Locate every leukocyte (white blood cell).
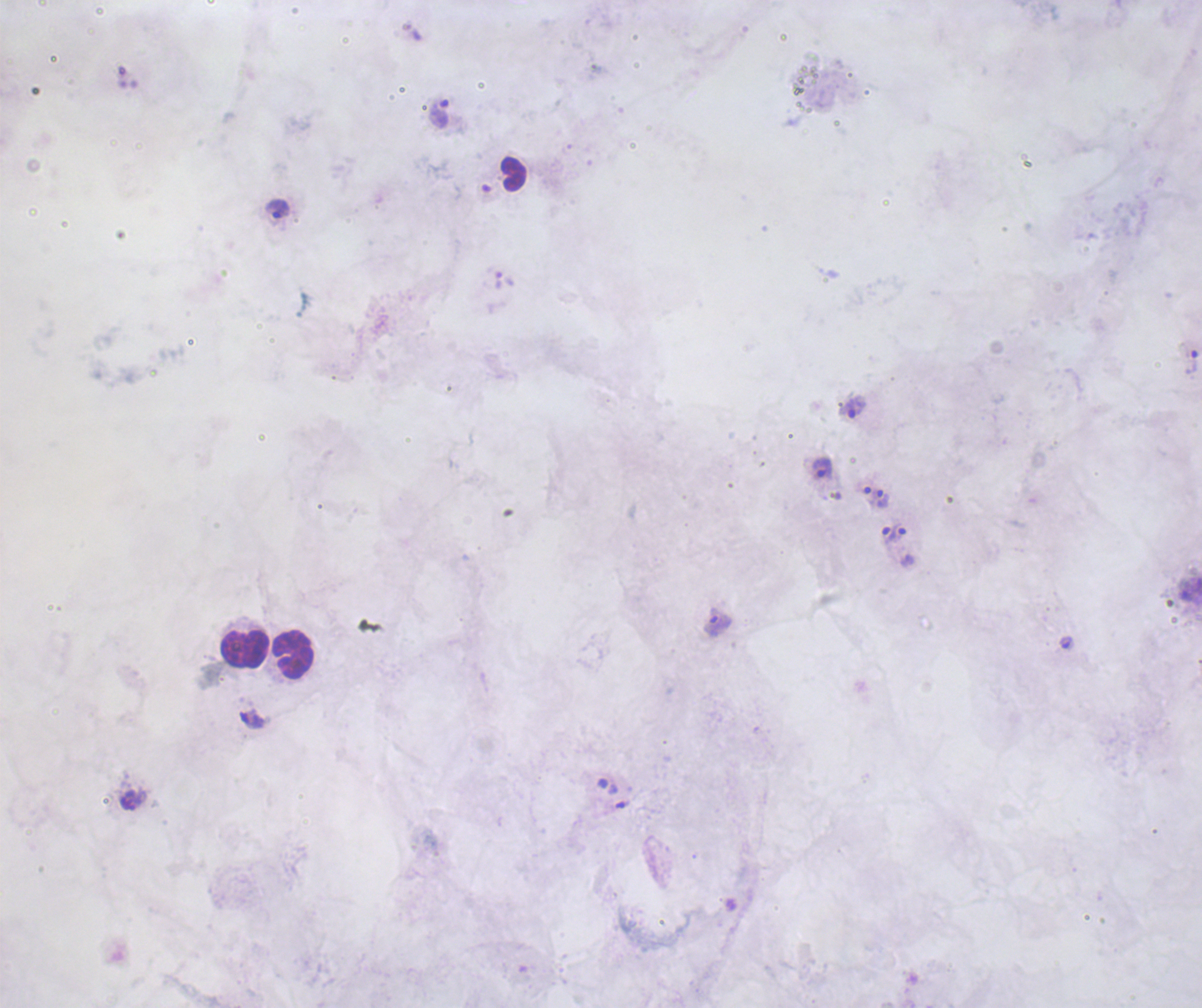
Approximate centers as {x, y} in pixels.
Leukocytes: {513, 174}, {245, 648}, {292, 655}.

Approximate centers as {x, y} in pixels. Trophozoite locations: {439, 114}, {277, 208}, {1193, 362}, {852, 408}, {824, 468}, {883, 498}, {899, 532}, {887, 535}, {715, 623}, {1066, 642}, {252, 719}. Single field of view. Captured at 100x magnification. Thick blood film. Romanowsky-stained preparation. Image is 1202×1008 pixels. Coloration quality: bad. Result: malaria parasites detected. Previously used in an actual diagnosis. Background quality: unsatisfactory.